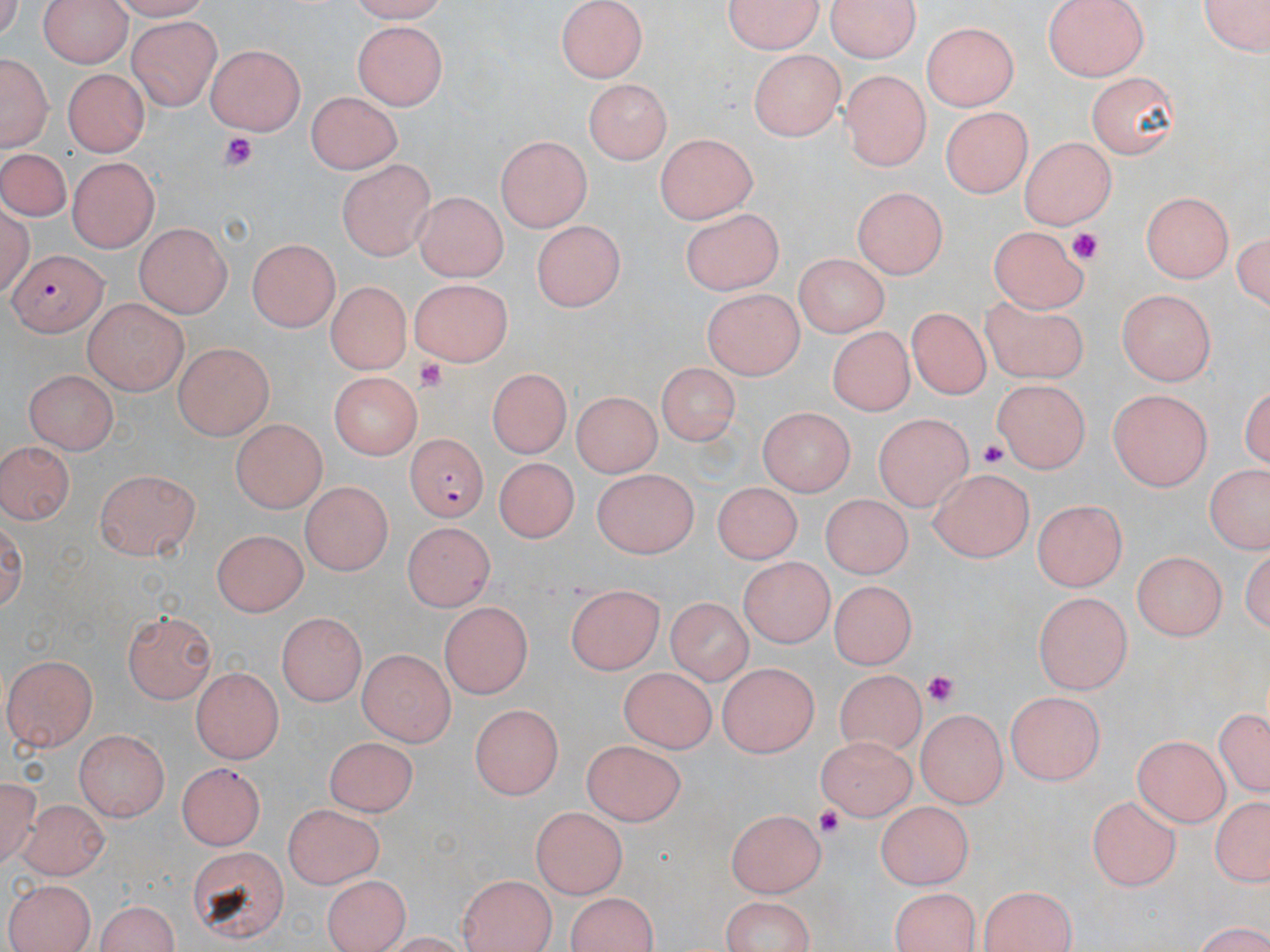

Approximate bounding boxes as named x1/y1/x2/y2 corners in pixels. Plasmodium falciparum-infected red blood cell locations: (x1=8, y1=248, x2=106, y2=334), (x1=402, y1=433, x2=490, y2=525). Platelet locations: (x1=219, y1=132, x2=257, y2=169), (x1=1067, y1=227, x2=1103, y2=260), (x1=415, y1=359, x2=449, y2=394), (x1=976, y1=436, x2=1013, y2=471), (x1=920, y1=670, x2=959, y2=706), (x1=813, y1=805, x2=846, y2=836). Uninfected red blood cell locations: (x1=37, y1=0, x2=134, y2=66), (x1=720, y1=0, x2=825, y2=55), (x1=828, y1=0, x2=921, y2=62), (x1=1043, y1=0, x2=1152, y2=82), (x1=1204, y1=0, x2=1269, y2=60), (x1=556, y1=2, x2=649, y2=83), (x1=130, y1=19, x2=221, y2=108), (x1=354, y1=21, x2=449, y2=110), (x1=923, y1=21, x2=1022, y2=111), (x1=206, y1=42, x2=307, y2=135), (x1=749, y1=50, x2=844, y2=141), (x1=1, y1=52, x2=49, y2=152), (x1=1085, y1=68, x2=1183, y2=157), (x1=62, y1=69, x2=148, y2=157), (x1=840, y1=69, x2=934, y2=168), (x1=585, y1=77, x2=673, y2=163), (x1=307, y1=92, x2=404, y2=173), (x1=941, y1=104, x2=1038, y2=197), (x1=652, y1=132, x2=757, y2=224), (x1=494, y1=135, x2=592, y2=231), (x1=1017, y1=135, x2=1116, y2=229), (x1=0, y1=146, x2=72, y2=222), (x1=68, y1=157, x2=160, y2=252), (x1=336, y1=160, x2=434, y2=260), (x1=851, y1=185, x2=945, y2=280), (x1=1142, y1=191, x2=1232, y2=284), (x1=415, y1=193, x2=507, y2=282), (x1=681, y1=208, x2=784, y2=297), (x1=533, y1=222, x2=620, y2=313), (x1=134, y1=223, x2=233, y2=317), (x1=987, y1=224, x2=1090, y2=313), (x1=1232, y1=229, x2=1268, y2=318), (x1=247, y1=238, x2=341, y2=331), (x1=788, y1=254, x2=888, y2=335), (x1=404, y1=280, x2=513, y2=369), (x1=326, y1=282, x2=407, y2=375), (x1=699, y1=287, x2=804, y2=378), (x1=1115, y1=289, x2=1218, y2=383), (x1=980, y1=295, x2=1092, y2=387), (x1=82, y1=298, x2=186, y2=397), (x1=908, y1=304, x2=990, y2=404), (x1=828, y1=327, x2=914, y2=415), (x1=173, y1=343, x2=275, y2=437), (x1=656, y1=362, x2=738, y2=448), (x1=25, y1=367, x2=120, y2=454), (x1=484, y1=369, x2=572, y2=459), (x1=325, y1=371, x2=424, y2=460), (x1=991, y1=381, x2=1090, y2=475), (x1=1106, y1=390, x2=1217, y2=491), (x1=571, y1=391, x2=660, y2=479), (x1=755, y1=411, x2=854, y2=495), (x1=871, y1=413, x2=974, y2=507), (x1=231, y1=417, x2=325, y2=512), (x1=2, y1=438, x2=73, y2=530), (x1=492, y1=457, x2=586, y2=542), (x1=93, y1=466, x2=202, y2=558), (x1=927, y1=466, x2=1033, y2=562), (x1=1201, y1=467, x2=1270, y2=557), (x1=592, y1=468, x2=697, y2=558), (x1=298, y1=479, x2=389, y2=574), (x1=710, y1=482, x2=803, y2=564), (x1=822, y1=493, x2=909, y2=580), (x1=1035, y1=501, x2=1129, y2=588), (x1=399, y1=524, x2=491, y2=613), (x1=212, y1=530, x2=306, y2=618), (x1=1132, y1=549, x2=1225, y2=642), (x1=738, y1=557, x2=836, y2=644), (x1=828, y1=582, x2=916, y2=671), (x1=566, y1=586, x2=663, y2=676), (x1=1032, y1=592, x2=1130, y2=691), (x1=663, y1=599, x2=748, y2=684), (x1=438, y1=604, x2=533, y2=697), (x1=123, y1=610, x2=217, y2=703), (x1=275, y1=612, x2=364, y2=707), (x1=356, y1=649, x2=458, y2=742), (x1=6, y1=654, x2=100, y2=751), (x1=717, y1=662, x2=816, y2=758), (x1=835, y1=664, x2=920, y2=749), (x1=617, y1=666, x2=717, y2=755), (x1=191, y1=668, x2=285, y2=763), (x1=1006, y1=691, x2=1101, y2=785), (x1=1212, y1=703, x2=1269, y2=801), (x1=469, y1=704, x2=560, y2=800), (x1=917, y1=707, x2=1005, y2=808), (x1=75, y1=729, x2=169, y2=822), (x1=815, y1=735, x2=918, y2=817), (x1=1130, y1=735, x2=1231, y2=823), (x1=324, y1=736, x2=418, y2=814), (x1=583, y1=738, x2=688, y2=822), (x1=176, y1=763, x2=266, y2=848), (x1=0, y1=774, x2=40, y2=869), (x1=1085, y1=795, x2=1181, y2=887), (x1=1206, y1=797, x2=1270, y2=887), (x1=19, y1=798, x2=111, y2=879), (x1=871, y1=800, x2=976, y2=888), (x1=279, y1=804, x2=387, y2=888), (x1=532, y1=808, x2=624, y2=900), (x1=728, y1=809, x2=826, y2=894), (x1=17, y1=835, x2=109, y2=945), (x1=187, y1=845, x2=289, y2=944), (x1=321, y1=873, x2=409, y2=950), (x1=454, y1=873, x2=562, y2=952), (x1=3, y1=878, x2=94, y2=952), (x1=977, y1=885, x2=1077, y2=951), (x1=887, y1=886, x2=982, y2=950), (x1=561, y1=892, x2=660, y2=951), (x1=717, y1=893, x2=819, y2=951), (x1=90, y1=897, x2=183, y2=952). Slide-level diagnosis: Plasmodium falciparum. 1000x magnification. One field of a larger specimen. Thin blood film. Image is 1270×952 pixels. May-Grünwald-Giemsa stain. Optical microscopy.